Outline each Plasmodium falciparum-infected red blood cell.
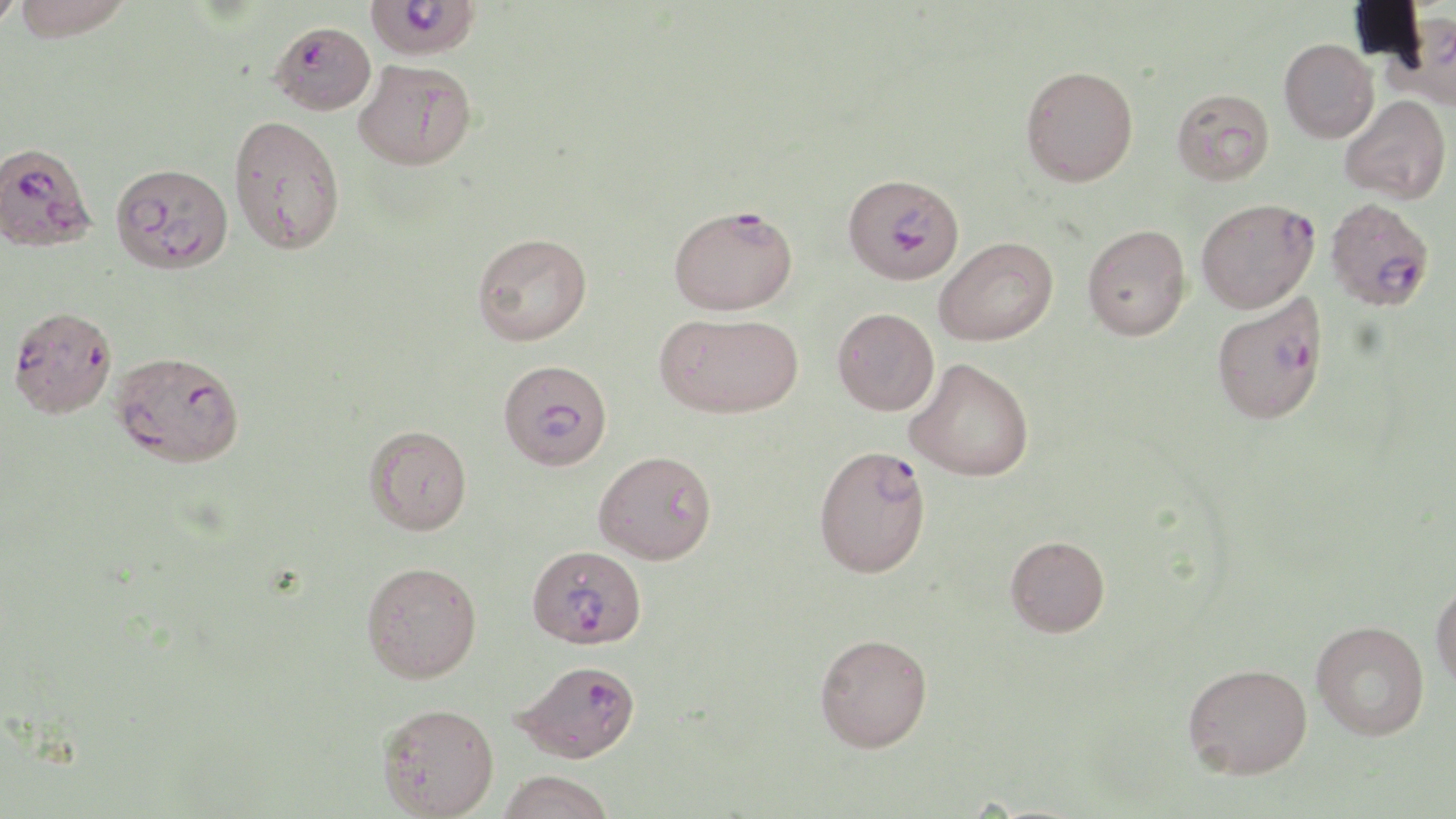
Approximate bounding boxes as [x1, y1, x2, y2] in pixels.
Plasmodium falciparum-infected red blood cells: [363, 0, 481, 62], [270, 21, 377, 116], [0, 141, 97, 253], [111, 162, 233, 273], [842, 172, 964, 285], [1325, 196, 1435, 311], [1196, 198, 1320, 314], [669, 204, 797, 315], [1211, 293, 1328, 425], [8, 305, 117, 419], [110, 349, 245, 468], [497, 368, 611, 470], [813, 444, 931, 578], [527, 544, 647, 645], [514, 660, 641, 764].

Uninfected red blood cell locations: [0, 0, 24, 31], [12, 0, 134, 40], [1385, 11, 1456, 111], [1279, 38, 1379, 143], [353, 58, 476, 171], [1020, 65, 1138, 186], [1171, 88, 1274, 186], [1339, 94, 1452, 204], [228, 114, 345, 255], [1081, 224, 1191, 340], [473, 232, 592, 345], [935, 236, 1058, 346], [832, 307, 940, 415], [655, 312, 802, 418], [904, 357, 1034, 481], [364, 425, 472, 535], [593, 450, 717, 565], [1005, 535, 1110, 637], [361, 560, 482, 683], [1430, 577, 1456, 693], [1311, 620, 1430, 740], [815, 632, 933, 752], [1182, 662, 1312, 779], [377, 702, 500, 818], [497, 770, 616, 819]. Slide-level diagnosis: Plasmodium falciparum. Optical microscopy. Image is 1456×819 pixels. Captured at 1000x magnification. May-Grünwald-Giemsa-stained preparation. Thin blood film. Single field of view.